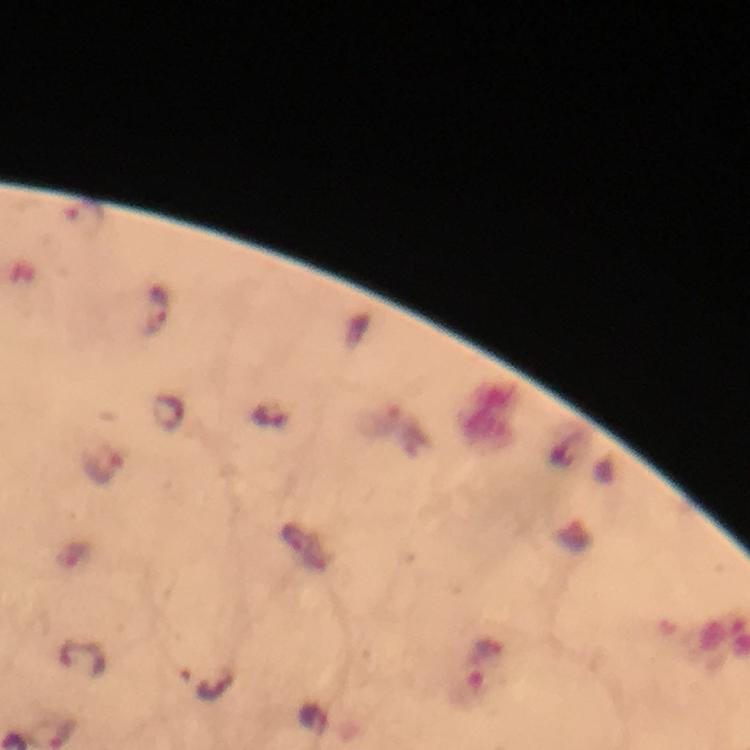

Approximate centers as (x, y) in pixels. Malaria parasite locations: (158, 308), (103, 463), (483, 666). Thick blood film. Image is 750×750 pixels. 100x magnification. Giemsa stain. From a malaria diagnostic workup. A crop from one field of view. Immersion oil applied. Smartphone photograph taken through a microscope.